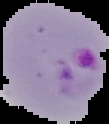 The area outside the segmented cell region is set to black. Malaria status: parasitized. Image is 109×124 pixels. From a thin blood smear.